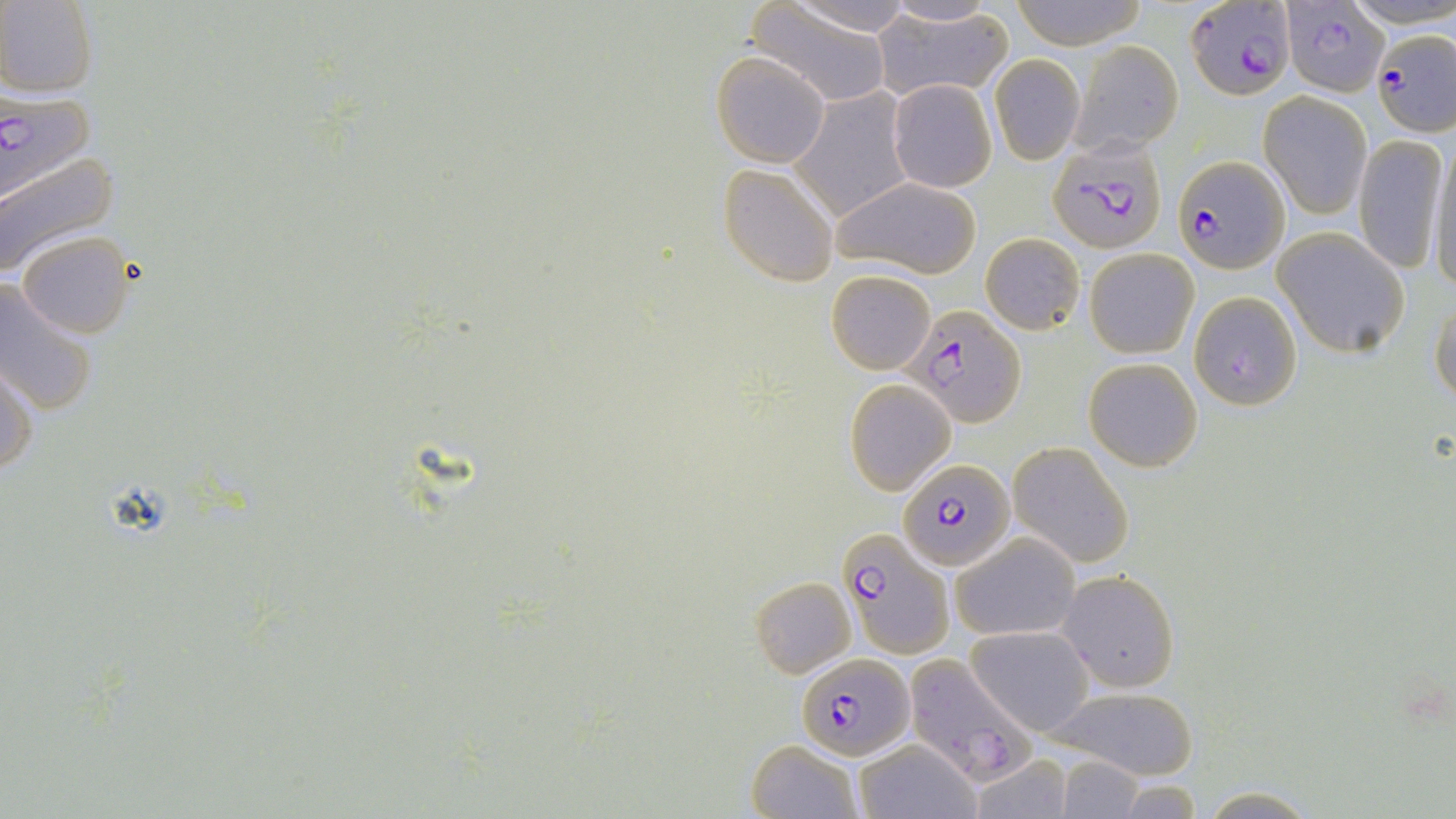

Approximate bounding boxes as (x1,y1)-(x2,y2) corner pairs in pixels. Plasmodium falciparum-infected red blood cell locations: (1189,1)-(1295,98), (1281,4)-(1388,95), (1373,27)-(1455,137), (0,84)-(93,202), (1045,134)-(1169,254), (1173,154)-(1290,274), (1189,291)-(1303,412), (906,303)-(1024,428), (899,461)-(1015,572), (837,529)-(953,657), (798,653)-(915,760), (905,653)-(1034,785). Uninfected red blood cell locations: (0,0)-(98,97), (782,0)-(917,36), (1012,0)-(1146,50), (746,1)-(895,108), (870,6)-(1015,102), (1070,38)-(1184,157), (710,50)-(831,168), (988,54)-(1084,165), (887,78)-(997,193), (792,89)-(914,222), (1260,91)-(1373,217), (1353,132)-(1448,278), (1425,142)-(1455,292), (0,154)-(121,279), (717,163)-(839,286), (830,177)-(981,277), (1272,227)-(1411,357), (17,231)-(136,339), (981,233)-(1084,335), (1084,247)-(1198,358), (825,271)-(936,375), (0,277)-(99,419), (1430,295)-(1456,409), (1082,357)-(1203,471), (1,358)-(37,478), (843,379)-(954,494), (1009,441)-(1133,565), (949,531)-(1079,642), (1058,570)-(1178,692), (750,576)-(856,676), (966,625)-(1094,737), (1047,682)-(1202,779), (852,738)-(982,819), (745,739)-(865,819), (967,752)-(1073,819), (1055,758)-(1143,818), (1196,786)-(1323,818). Slide-level diagnosis: Plasmodium falciparum. Thin blood film. Image is 1456×819 pixels. Single field of view. Light microscopy. 1000x magnification. May-Grünwald-Giemsa-stained preparation.